Describe the morphology of the red blood cells.
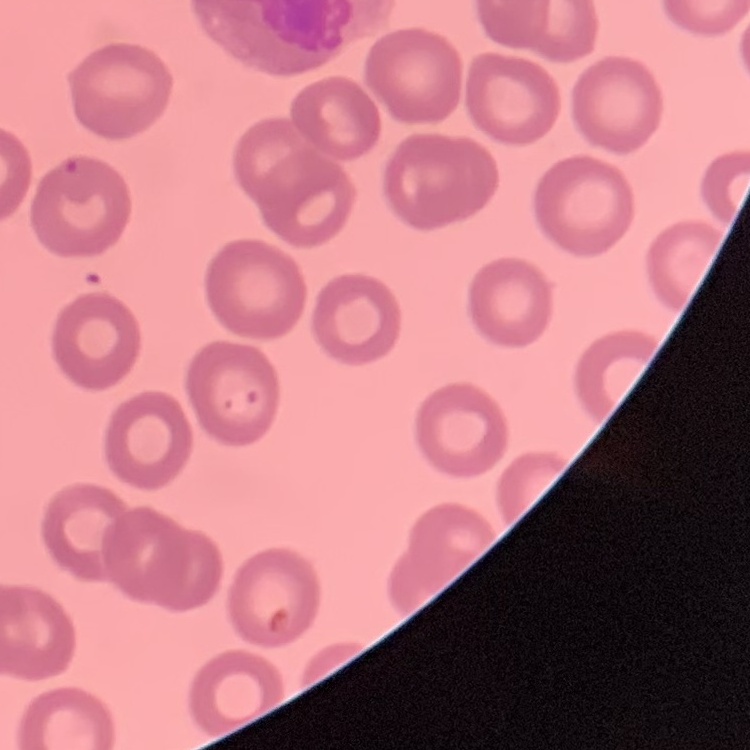

They show no rouleaux formation.

Thin blood smear. One tile cut from a larger photomicrograph. Field's or Giemsa stain.